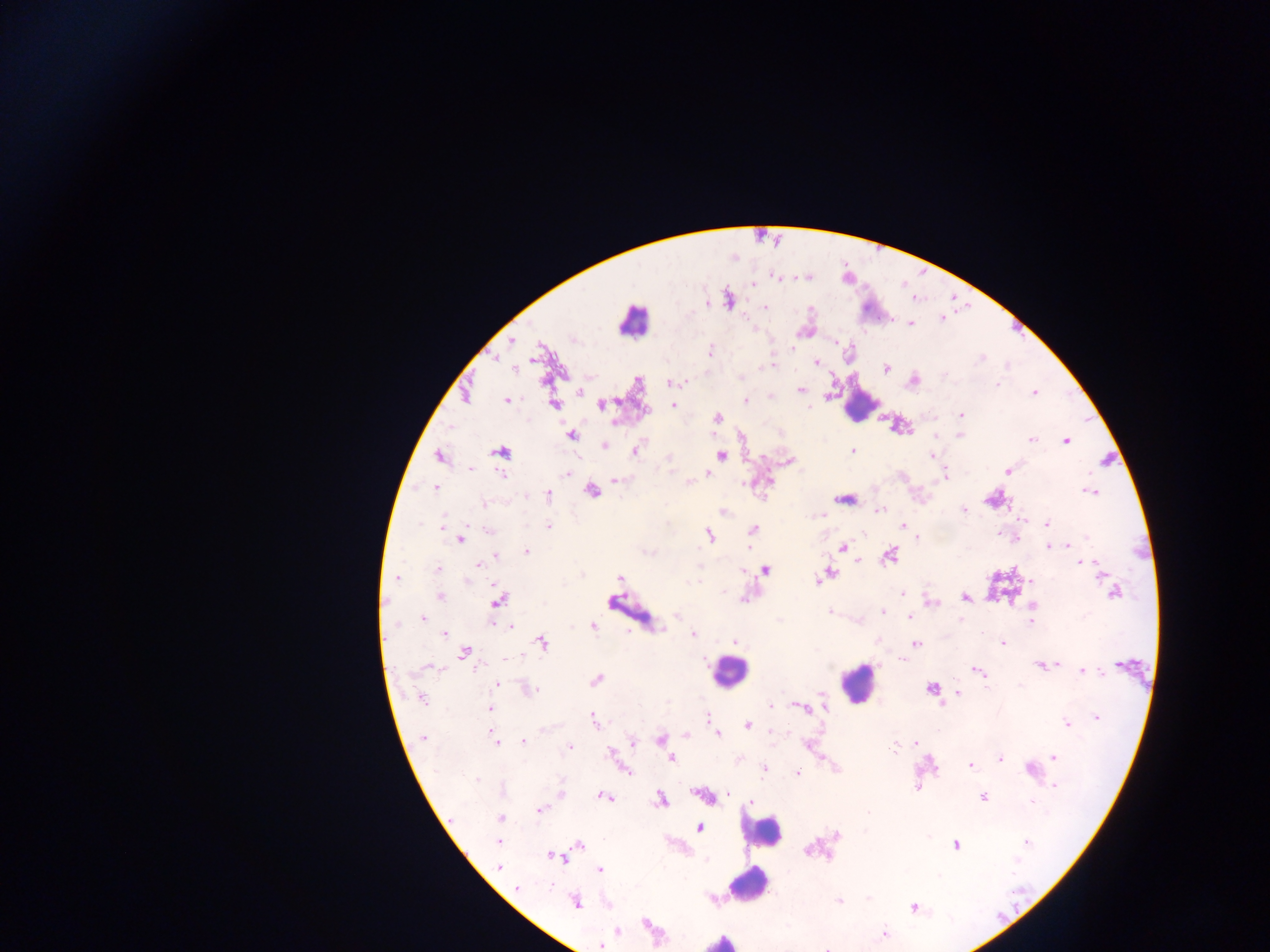

Approximate centers as (x, y) in pixels.
Summary:
  - Leukocyte locations: (633, 320), (859, 405), (728, 671), (856, 683), (762, 830), (748, 884), (721, 940)
  - Malaria parasite locations: (806, 277), (777, 278), (751, 282), (729, 299), (765, 306), (941, 319), (910, 324), (805, 330), (511, 341), (835, 343), (710, 351), (496, 359), (815, 362), (513, 368), (885, 368), (913, 380), (670, 382), (997, 385), (579, 391), (800, 391), (1034, 392), (464, 394), (506, 400), (745, 401), (554, 404), (601, 404), (673, 405), (962, 415), (717, 418), (899, 425), (571, 435), (959, 435), (1030, 438), (1066, 440), (604, 445), (635, 448), (852, 450), (501, 451), (721, 455), (932, 455), (438, 456), (789, 461), (1007, 470), (566, 473), (709, 474), (945, 476), (616, 479), (688, 482), (435, 487), (591, 491), (1089, 491), (548, 495), (844, 499), (994, 499), (963, 510), (724, 511), (878, 511), (820, 516), (1021, 520), (1047, 523), (442, 526), (549, 526), (902, 527), (752, 530), (489, 531), (709, 535), (460, 538), (1068, 545), (1048, 546), (841, 548), (526, 551), (890, 554), (496, 556), (857, 560), (1080, 562), (479, 565), (436, 568), (764, 569), (829, 573), (1103, 573), (581, 574), (824, 576), (396, 578), (620, 578), (819, 581), (901, 592), (1114, 592), (441, 596), (964, 597), (613, 600), (498, 601), (930, 602), (1031, 605), (830, 611), (883, 613), (677, 615), (909, 615), (423, 618), (1030, 622), (510, 625), (592, 625), (444, 633), (693, 634), (734, 640), (542, 642), (1001, 643), (916, 645), (464, 652), (504, 660), (1042, 665), (1122, 665), (976, 671), (1082, 671), (596, 680), (496, 684), (932, 688), (526, 689), (956, 693), (821, 696), (421, 697), (823, 705), (801, 706), (488, 709), (1096, 716), (709, 717), (594, 720), (1066, 724), (747, 725), (718, 734), (685, 735), (423, 737), (493, 738), (661, 739), (523, 741), (632, 741), (915, 742), (569, 747), (612, 755), (1053, 757), (671, 758), (999, 759), (970, 765), (764, 768), (624, 769), (1030, 769), (797, 772), (1053, 785), (916, 788), (560, 794), (704, 795), (603, 796), (982, 797), (661, 799), (750, 801), (538, 810), (500, 819), (699, 827), (836, 835), (498, 841), (1026, 842), (578, 844), (956, 845), (554, 856), (497, 866), (599, 870), (517, 888), (712, 898), (869, 899), (838, 901), (575, 902), (914, 906), (616, 931), (883, 933), (600, 945), (829, 946)
  - Field of view: single
  - Capture: mobile-phone photograph through a microscope
  - Country: Ghana
  - Image size: 1270×952 pixels
  - Preparation: thick blood smear